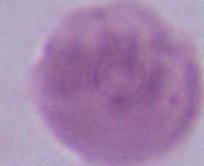
A red blood cell is seen. Micrograph. Captured at 1000x magnification.